Assess the morphology of the erythrocytes.
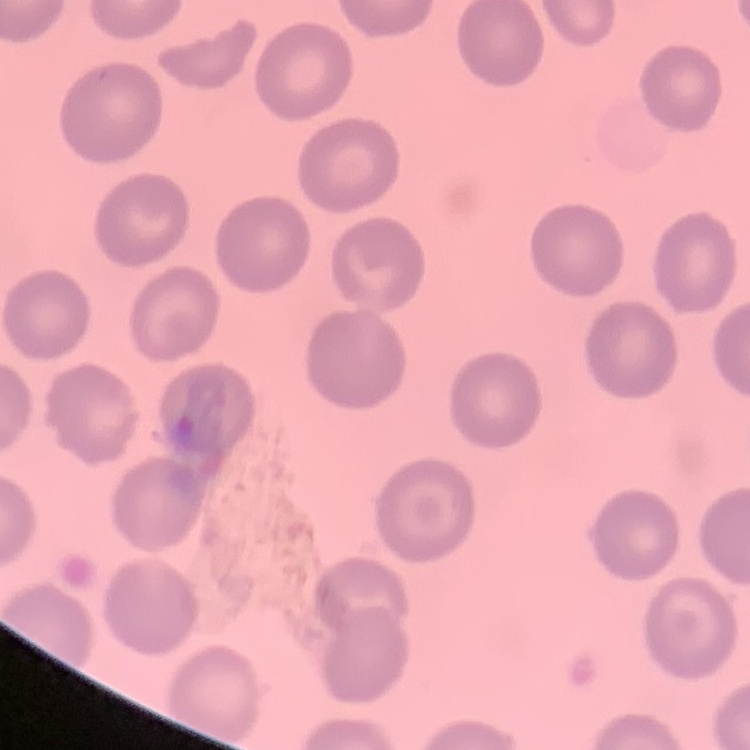

They show no rouleaux formation.

image type = one tile cut from a larger photomicrograph
preparation = thin blood smear
stain = Field's or Giemsa